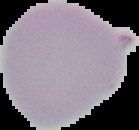 Image is 139×130 pixels. Cell region segmented out of the field of view; the surrounding area is masked to black. Malaria status: uninfected. From a thin blood smear.